Describe the morphology of the red blood cells.
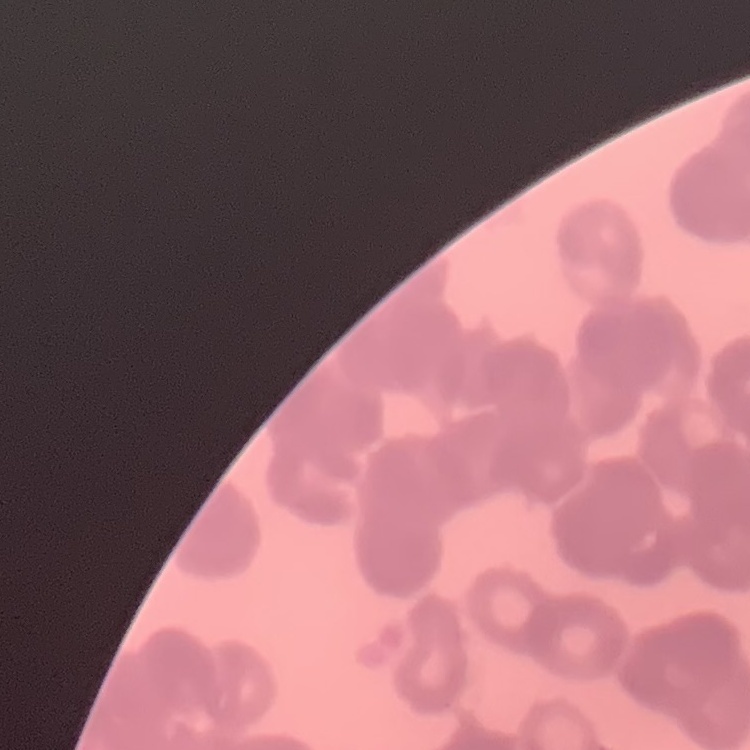
They show rouleaux formation.

Summary:
  - Preparation: thin peripheral smear
  - Stain: Field's or Giemsa
  - Image type: square crop of a larger photomicrograph